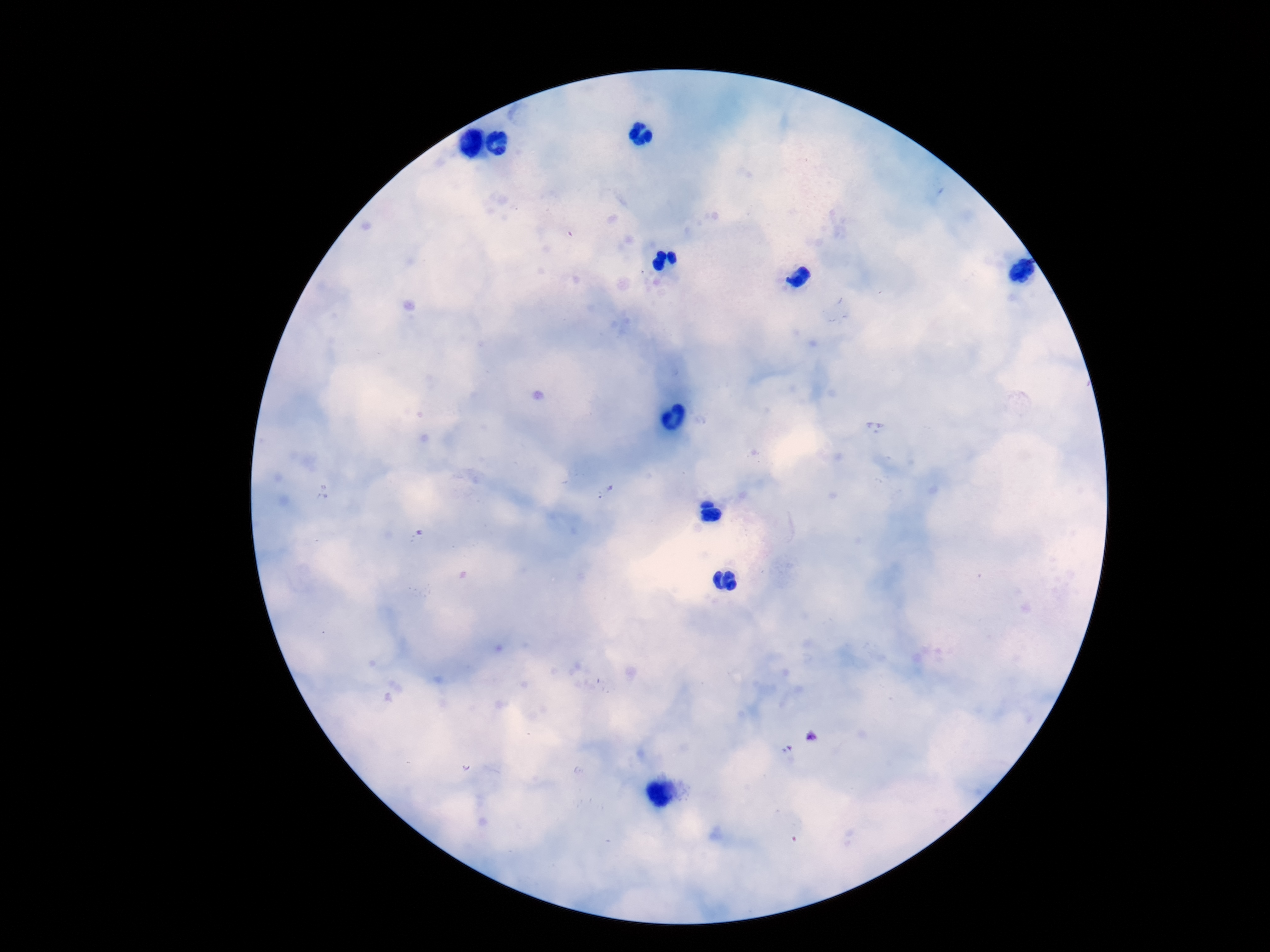

patient malaria status = infected
field of view = one from this slide
Plasmodium parasite locations = approximate centers as {x, y} in pixels: {606, 492}, {812, 737}
stain = Giemsa
image size = 1270×952 pixels
preparation = thick blood film
magnification = 100x
capture = smartphone camera through the microscope eyepiece